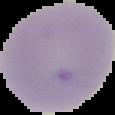

From a thin blood film. Result: negative for Plasmodium parasites. Cell region segmented out of the field of view; the surrounding area is masked to black. Image is 115×115 pixels.